Identify the blood parasite species.
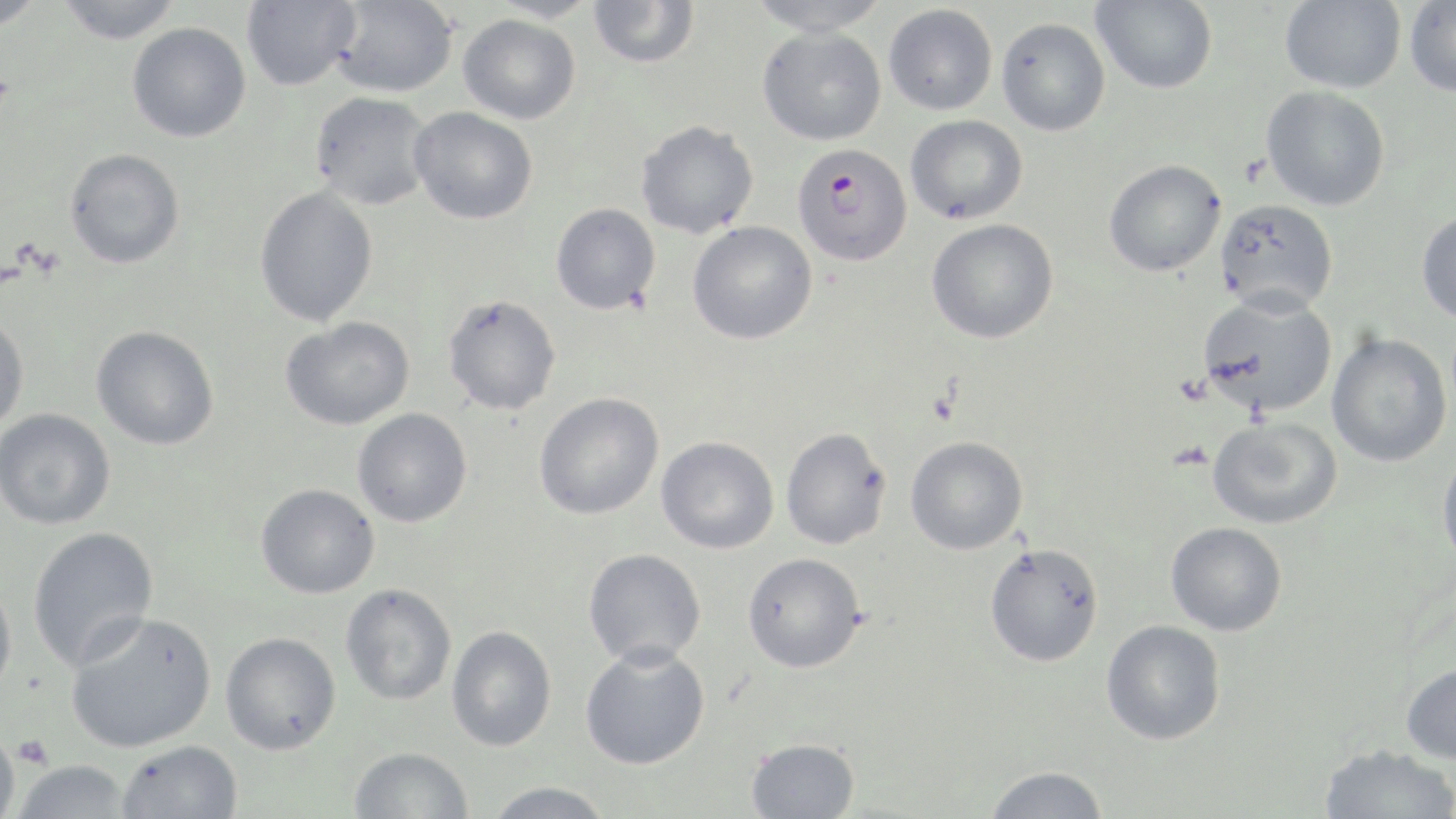

Plasmodium falciparum.

Approximate bounding boxes as named x1/y1/x2/y2 corners in pixels. Platelet locations: (x1=13, y1=734, x2=53, y2=771). Uninfected red blood cell locations: (x1=0, y1=0, x2=47, y2=31), (x1=55, y1=0, x2=183, y2=44), (x1=242, y1=0, x2=361, y2=90), (x1=329, y1=0, x2=460, y2=98), (x1=486, y1=0, x2=600, y2=24), (x1=745, y1=0, x2=893, y2=37), (x1=1091, y1=0, x2=1218, y2=94), (x1=1280, y1=0, x2=1406, y2=93), (x1=588, y1=1, x2=700, y2=69), (x1=1404, y1=1, x2=1456, y2=99), (x1=883, y1=4, x2=998, y2=115), (x1=458, y1=14, x2=581, y2=125), (x1=996, y1=17, x2=1110, y2=136), (x1=127, y1=22, x2=251, y2=142), (x1=758, y1=26, x2=887, y2=146), (x1=1261, y1=85, x2=1390, y2=211), (x1=309, y1=92, x2=434, y2=211), (x1=409, y1=106, x2=538, y2=225), (x1=905, y1=114, x2=1028, y2=225), (x1=635, y1=120, x2=760, y2=239), (x1=64, y1=148, x2=185, y2=269), (x1=1103, y1=159, x2=1227, y2=277), (x1=254, y1=185, x2=378, y2=327), (x1=1214, y1=199, x2=1339, y2=316), (x1=551, y1=203, x2=661, y2=314), (x1=1416, y1=209, x2=1456, y2=326), (x1=926, y1=218, x2=1059, y2=344), (x1=687, y1=221, x2=817, y2=345), (x1=1196, y1=292, x2=1338, y2=418), (x1=442, y1=294, x2=562, y2=416), (x1=0, y1=314, x2=29, y2=432), (x1=280, y1=316, x2=415, y2=430), (x1=91, y1=325, x2=219, y2=450), (x1=1327, y1=333, x2=1452, y2=467), (x1=533, y1=392, x2=664, y2=520), (x1=0, y1=408, x2=116, y2=530), (x1=352, y1=408, x2=472, y2=527), (x1=1207, y1=416, x2=1342, y2=530), (x1=780, y1=427, x2=891, y2=550), (x1=905, y1=435, x2=1028, y2=554), (x1=656, y1=437, x2=779, y2=554), (x1=1437, y1=450, x2=1456, y2=570), (x1=256, y1=484, x2=380, y2=598), (x1=1166, y1=522, x2=1287, y2=636), (x1=27, y1=526, x2=158, y2=670), (x1=984, y1=542, x2=1104, y2=667), (x1=583, y1=548, x2=706, y2=668), (x1=742, y1=552, x2=866, y2=672), (x1=0, y1=576, x2=18, y2=700), (x1=340, y1=583, x2=457, y2=705), (x1=65, y1=611, x2=217, y2=753), (x1=1101, y1=620, x2=1226, y2=745), (x1=446, y1=625, x2=557, y2=751), (x1=220, y1=632, x2=341, y2=755), (x1=580, y1=643, x2=710, y2=770), (x1=1399, y1=662, x2=1456, y2=764), (x1=0, y1=728, x2=20, y2=819), (x1=745, y1=737, x2=860, y2=818), (x1=117, y1=740, x2=243, y2=819), (x1=1318, y1=744, x2=1456, y2=819), (x1=348, y1=746, x2=473, y2=819), (x1=11, y1=759, x2=133, y2=818), (x1=982, y1=765, x2=1110, y2=819), (x1=482, y1=782, x2=615, y2=818). Plasmodium falciparum-infected red blood cell locations: (x1=792, y1=142, x2=909, y2=267). May-Grünwald-Giemsa stain. Single field of view. Thin blood film. Image is 1456×819 pixels. 1000x magnification. Light microscopy.